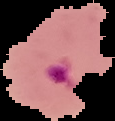
preparation: thin blood film
image_size: 115×121 pixels
image_type: segmented cell region on a black background
result: Plasmodium parasites identified